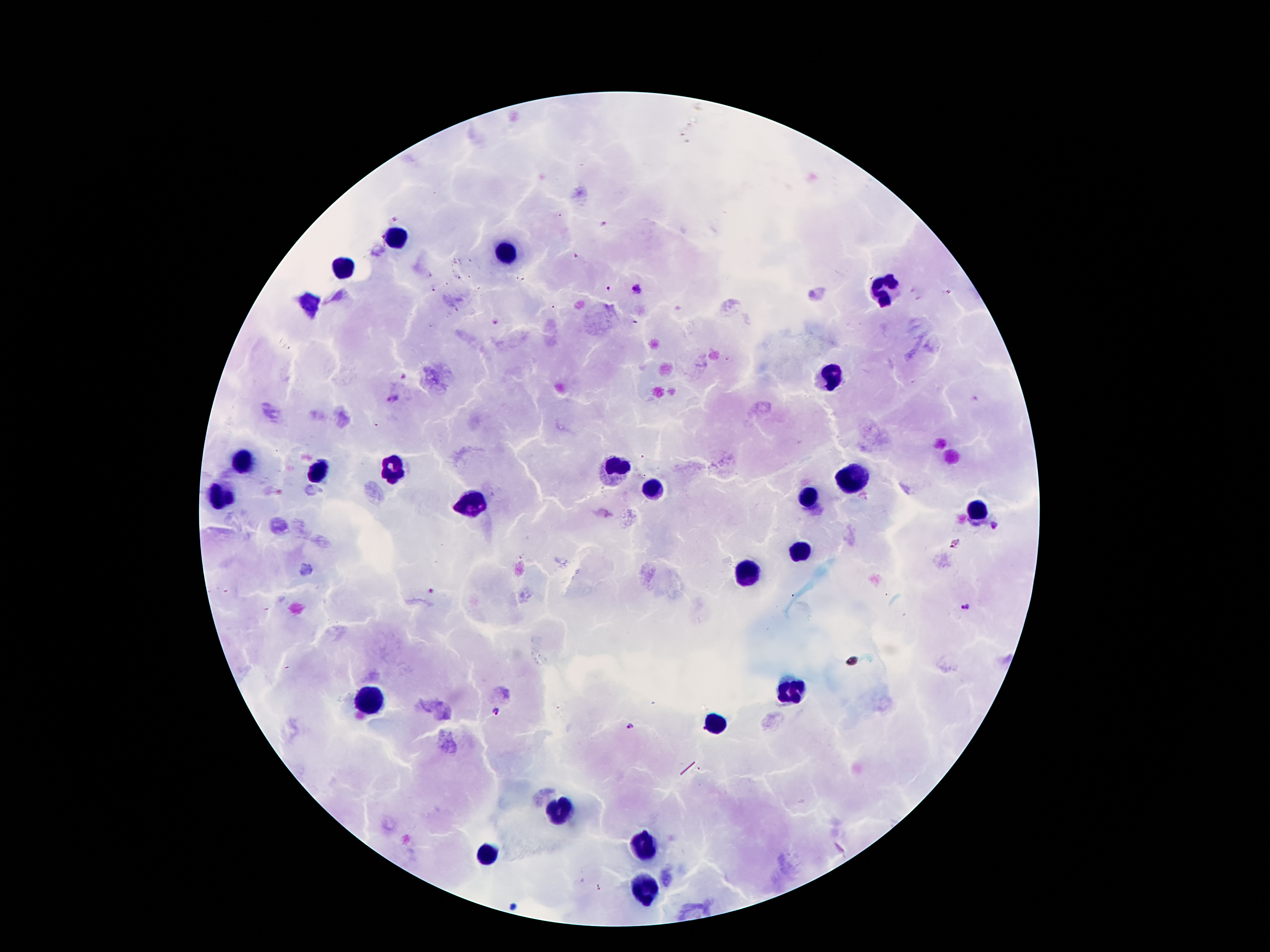

Approximate centers as [x, y] in pixels.
Summary:
  - Leukocyte locations: [395, 238], [507, 250], [344, 268], [882, 287], [833, 377], [245, 461], [618, 467], [395, 469], [317, 471], [850, 478], [651, 488], [809, 496], [217, 498], [475, 502], [977, 508], [800, 551], [749, 570], [792, 685], [368, 699], [718, 724], [563, 806], [641, 847], [487, 855], [643, 890]
  - Malaria parasite locations: [636, 290], [403, 375], [392, 400], [994, 526], [966, 605], [498, 712], [630, 725]
  - Field of view: one from this slide
  - Patient malaria status: positive for Plasmodium falciparum
  - Preparation: thick peripheral-blood smear
  - Capture: smartphone through the microscope eyepiece
  - Magnification: 100x
  - Stain: Giemsa
  - Image size: 1270×952 pixels